Identify the blood parasite species.
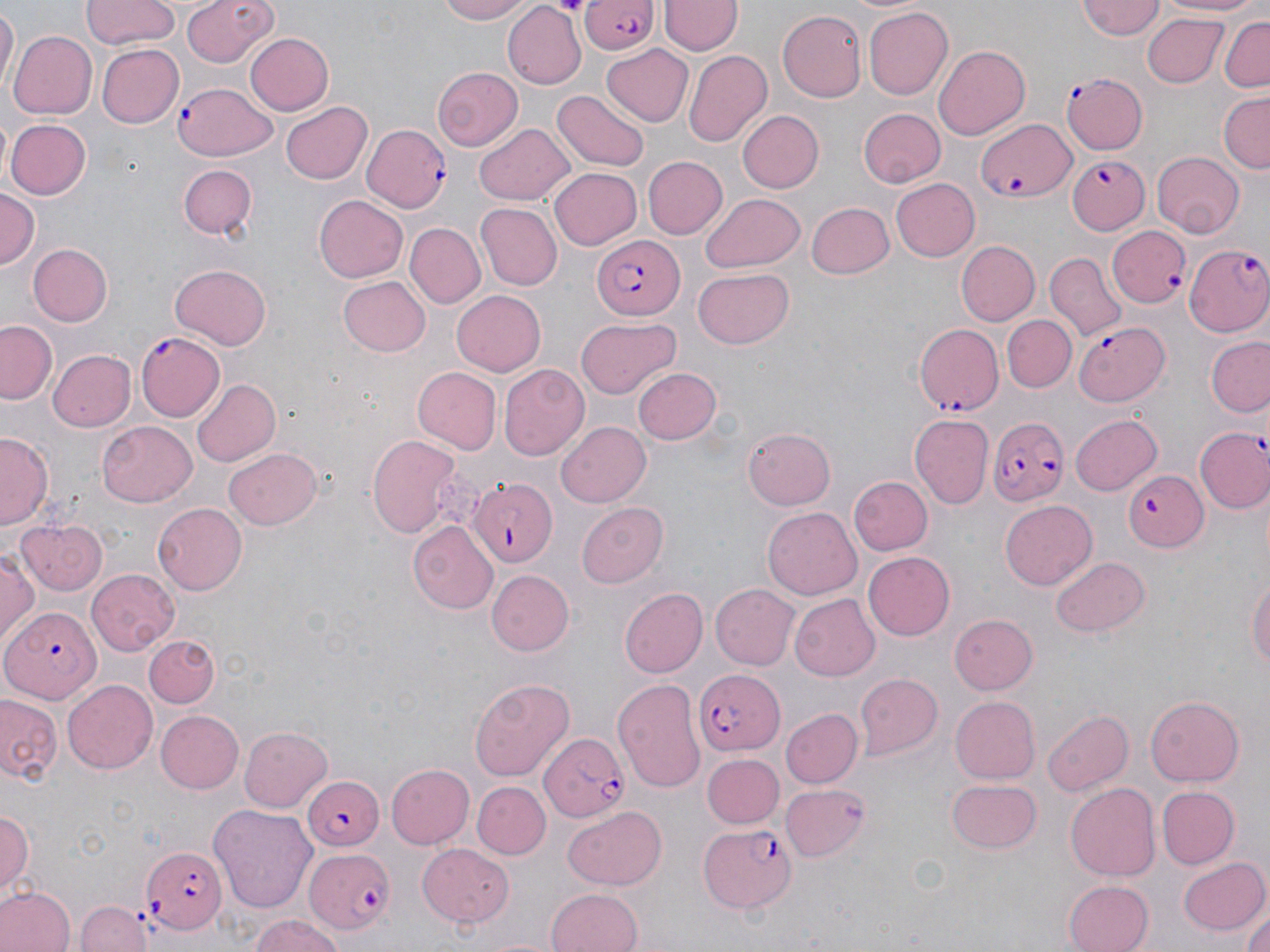
Plasmodium falciparum.

field_of_view: one of a larger specimen
modality: optical microscopy
image_size: 1270×952 pixels
preparation: thin blood smear
plasmodium_falciparum_infected_red_blood_cell_locations: 'approximate bounding boxes as [x1, y1, x2, y2] in pixels: [579, 0, 660, 54], [1062, 73, 1149, 156], [172, 79, 276, 160], [976, 115, 1076, 203], [361, 124, 454, 212], [1059, 151, 1150, 239], [1107, 225, 1192, 309], [593, 236, 684, 319], [1186, 243, 1270, 334], [914, 318, 1002, 423], [1071, 322, 1167, 407], [137, 332, 227, 421], [986, 415, 1069, 507], [1194, 425, 1270, 515], [1124, 469, 1209, 551], [468, 474, 558, 567], [3, 607, 101, 702], [692, 668, 782, 756], [537, 731, 625, 821], [299, 774, 385, 849], [697, 823, 796, 910], [301, 843, 392, 935], [139, 844, 225, 934]'
uninfected_red_blood_cell_locations: 'approximate bounding boxes as [x1, y1, x2, y2] in pixels: [81, 0, 181, 49], [183, 0, 277, 68], [434, 0, 536, 24], [1155, 0, 1270, 18], [2, 1, 17, 93], [1076, 1, 1165, 42], [661, 2, 739, 56], [502, 3, 587, 89], [864, 6, 955, 100], [776, 10, 867, 103], [1143, 15, 1227, 88], [1217, 16, 1270, 95], [8, 29, 97, 120], [244, 32, 335, 115], [601, 42, 694, 126], [96, 45, 184, 128], [932, 45, 1030, 141], [684, 49, 774, 145], [432, 66, 523, 149], [552, 91, 648, 170], [1219, 92, 1269, 172], [279, 99, 373, 186], [858, 108, 947, 188], [739, 109, 824, 194], [7, 119, 91, 199], [475, 125, 575, 205], [1153, 150, 1246, 236], [645, 155, 727, 239], [175, 162, 260, 242], [550, 165, 643, 248], [891, 178, 979, 263], [0, 190, 39, 275], [702, 194, 805, 272], [314, 195, 408, 283], [805, 200, 896, 279], [474, 203, 561, 290], [406, 222, 486, 307], [957, 241, 1040, 326], [26, 242, 113, 327], [1046, 253, 1124, 337], [168, 263, 272, 349], [693, 268, 796, 350], [338, 275, 430, 357], [452, 287, 546, 374], [1003, 315, 1077, 392], [576, 317, 681, 397], [0, 320, 56, 405], [1207, 336, 1270, 417], [46, 348, 136, 433], [499, 364, 590, 460], [633, 365, 722, 445], [412, 368, 502, 455], [191, 378, 280, 467], [910, 414, 993, 509], [1071, 415, 1162, 496], [97, 422, 200, 507], [555, 422, 651, 507], [744, 425, 836, 509], [0, 432, 51, 528], [365, 432, 465, 538], [225, 448, 323, 530], [851, 475, 933, 554], [1000, 499, 1095, 590], [152, 502, 247, 595], [578, 503, 671, 588], [762, 509, 862, 600], [14, 517, 110, 596], [0, 521, 70, 621], [408, 522, 497, 613], [1, 549, 39, 647], [864, 551, 956, 641], [1052, 555, 1150, 637], [87, 568, 179, 654], [487, 570, 575, 656], [1247, 570, 1269, 681], [710, 582, 802, 669], [618, 588, 706, 679], [790, 594, 880, 679], [949, 612, 1039, 693], [144, 636, 220, 706], [853, 673, 941, 760], [471, 677, 575, 782], [613, 677, 706, 789], [63, 679, 157, 775], [0, 692, 63, 787], [948, 696, 1039, 784], [1147, 696, 1244, 788], [782, 708, 864, 788], [1044, 708, 1132, 796], [155, 709, 243, 793], [240, 725, 336, 811], [703, 752, 784, 829], [387, 764, 474, 848], [947, 778, 1042, 855], [474, 781, 550, 860], [1066, 782, 1163, 880], [780, 783, 870, 861], [1156, 786, 1239, 869], [562, 804, 666, 889], [210, 805, 317, 910], [1, 806, 34, 902], [417, 844, 516, 927], [1178, 856, 1268, 935], [1061, 878, 1153, 952], [1, 885, 73, 952], [546, 887, 645, 952], [78, 900, 153, 952], [1242, 911, 1269, 952], [244, 915, 349, 952]'
magnification: 1000x
stain: May-Grünwald-Giemsa